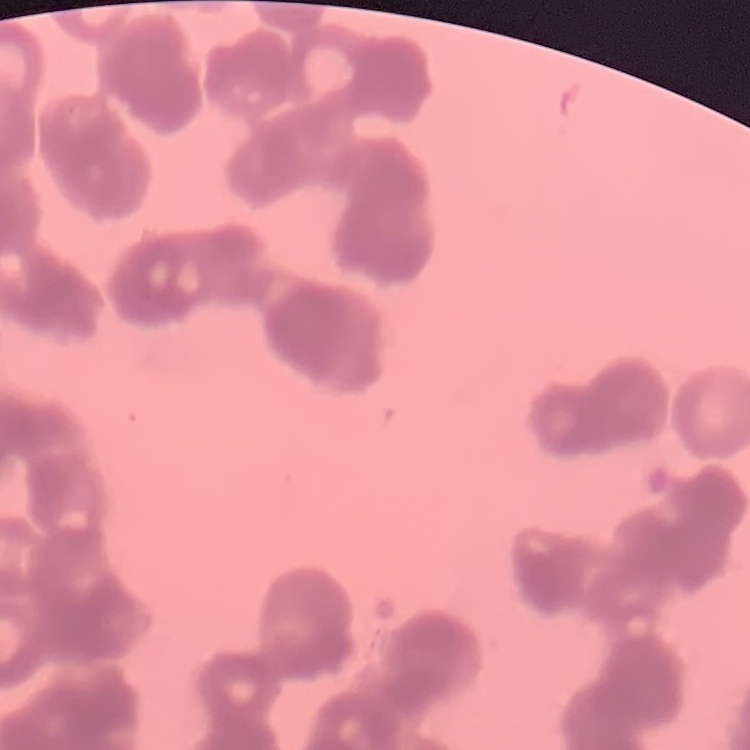

erythrocyte_morphology: rouleaux formation
stain: Field's or Giemsa
image_type: one tile cut from a larger photomicrograph
preparation: thin blood smear